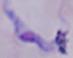 1000x magnification. A trypanosome is shown. Micrograph.